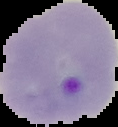
{
  "result": "Plasmodium parasites detected",
  "image_size": "118×127 pixels",
  "image_type": "cell region segmented out of the field of view; surrounding area masked to black",
  "preparation": "thin blood smear"
}